Describe the morphology of the erythrocytes.
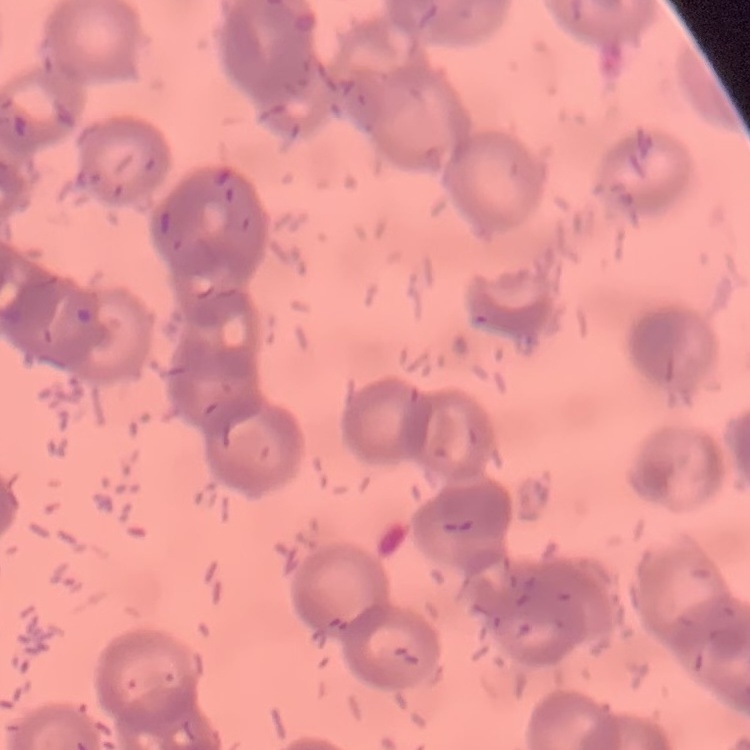

Rouleaux formation.

One tile cut from a larger photomicrograph. Field's or Giemsa stain. Thin peripheral smear.